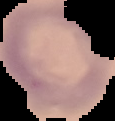

preparation = thin blood film
image size = 115×121 pixels
result = no malaria parasites seen
image type = segmented cell region with the area outside set to black